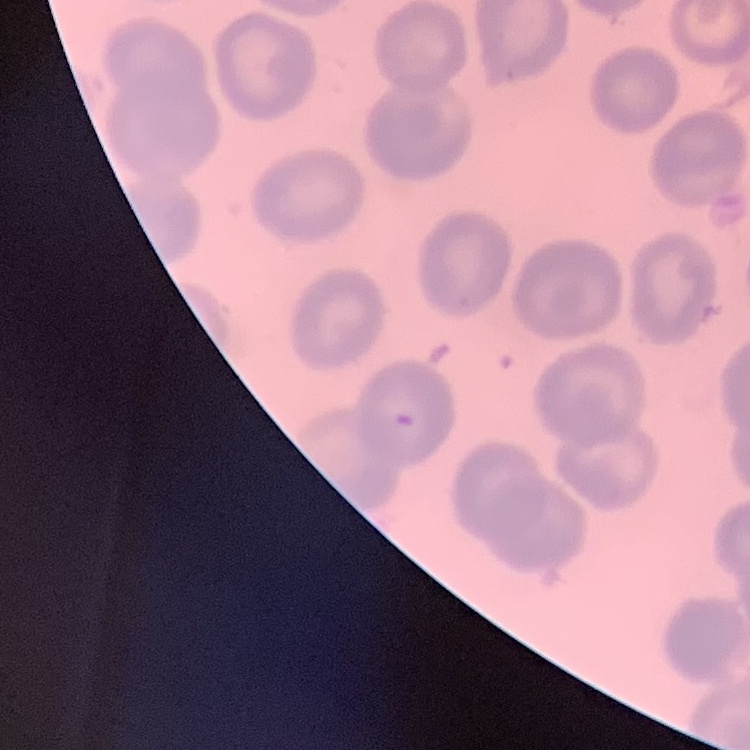

The red blood cells show no rouleaux formation. Field's or Giemsa stain. Square crop of a larger photomicrograph. Thin peripheral smear.